Identify the blood parasite species.
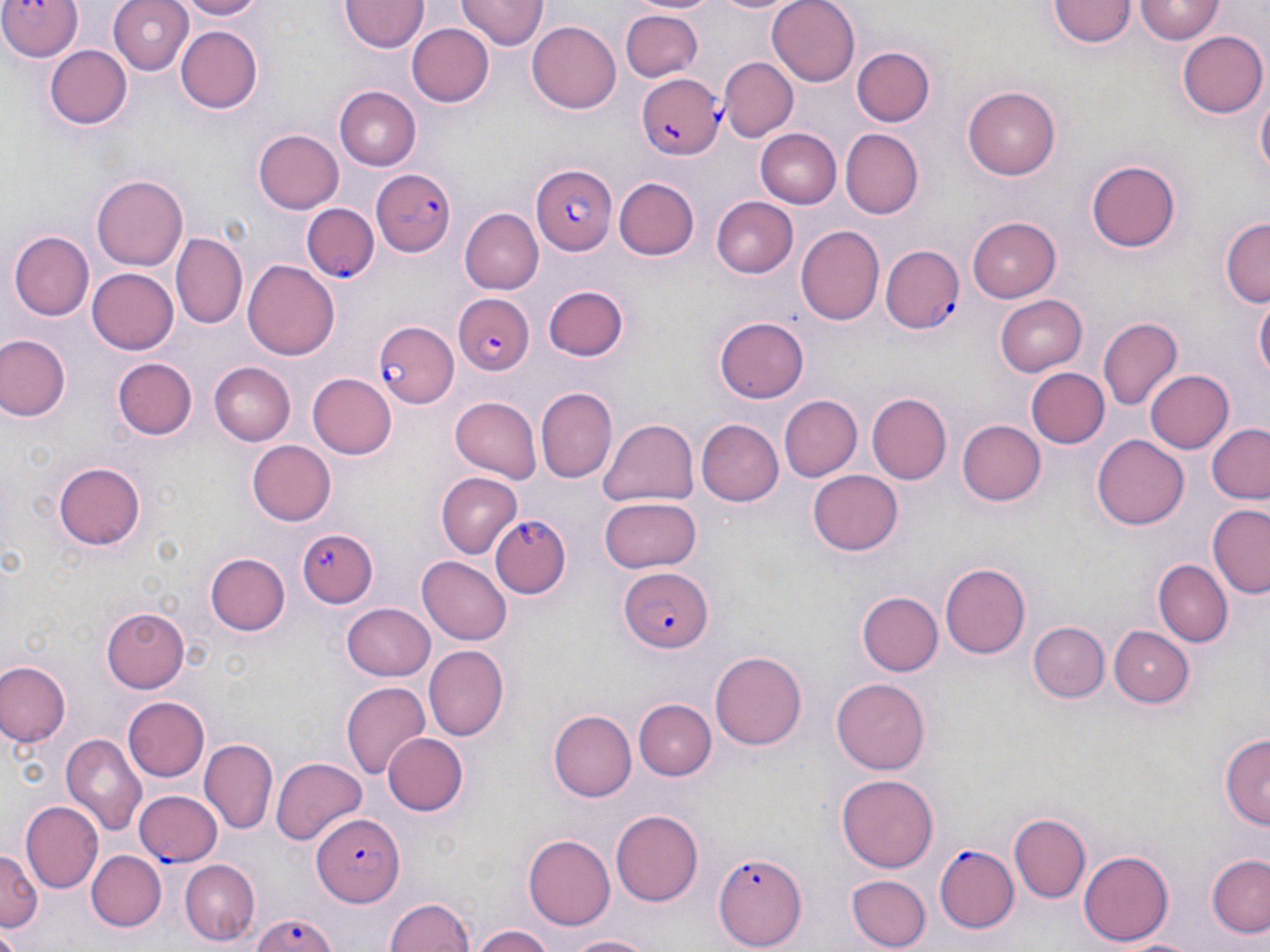

Plasmodium falciparum.

Approximate bounding boxes as named x1/y1/x2/y2 corners in pixels. Uninfected red blood cell locations: (x1=107, y1=0, x2=195, y2=74), (x1=175, y1=0, x2=265, y2=20), (x1=458, y1=0, x2=546, y2=52), (x1=635, y1=0, x2=718, y2=16), (x1=709, y1=0, x2=797, y2=16), (x1=767, y1=0, x2=861, y2=86), (x1=1051, y1=0, x2=1133, y2=49), (x1=1136, y1=1, x2=1224, y2=44), (x1=340, y1=2, x2=426, y2=54), (x1=620, y1=7, x2=702, y2=80), (x1=527, y1=21, x2=622, y2=113), (x1=408, y1=23, x2=494, y2=107), (x1=175, y1=24, x2=263, y2=114), (x1=1179, y1=30, x2=1268, y2=118), (x1=45, y1=43, x2=132, y2=130), (x1=851, y1=46, x2=936, y2=126), (x1=718, y1=57, x2=797, y2=142), (x1=964, y1=86, x2=1062, y2=179), (x1=334, y1=87, x2=420, y2=171), (x1=1255, y1=93, x2=1269, y2=184), (x1=840, y1=127, x2=923, y2=217), (x1=252, y1=129, x2=343, y2=214), (x1=755, y1=129, x2=842, y2=207), (x1=1087, y1=157, x2=1182, y2=251), (x1=93, y1=175, x2=188, y2=271), (x1=613, y1=177, x2=699, y2=261), (x1=710, y1=195, x2=797, y2=276), (x1=459, y1=206, x2=543, y2=291), (x1=966, y1=215, x2=1060, y2=304), (x1=1221, y1=219, x2=1269, y2=308), (x1=796, y1=226, x2=885, y2=327), (x1=172, y1=230, x2=246, y2=329), (x1=11, y1=231, x2=94, y2=320), (x1=244, y1=260, x2=339, y2=361), (x1=87, y1=267, x2=178, y2=355), (x1=543, y1=287, x2=627, y2=362), (x1=994, y1=292, x2=1088, y2=374), (x1=1255, y1=295, x2=1269, y2=386), (x1=713, y1=316, x2=809, y2=404), (x1=1099, y1=318, x2=1182, y2=410), (x1=0, y1=333, x2=70, y2=421), (x1=111, y1=356, x2=198, y2=443), (x1=206, y1=362, x2=295, y2=447), (x1=1027, y1=367, x2=1109, y2=449), (x1=1145, y1=369, x2=1235, y2=454), (x1=308, y1=373, x2=397, y2=459), (x1=537, y1=385, x2=616, y2=482), (x1=867, y1=392, x2=952, y2=483), (x1=779, y1=394, x2=861, y2=482), (x1=449, y1=397, x2=543, y2=482), (x1=598, y1=416, x2=699, y2=509), (x1=695, y1=420, x2=781, y2=505), (x1=955, y1=421, x2=1046, y2=508), (x1=1207, y1=424, x2=1270, y2=506), (x1=1092, y1=433, x2=1190, y2=530), (x1=246, y1=440, x2=337, y2=526), (x1=54, y1=462, x2=144, y2=550), (x1=808, y1=468, x2=904, y2=555), (x1=437, y1=473, x2=522, y2=558), (x1=599, y1=496, x2=703, y2=575), (x1=1207, y1=505, x2=1270, y2=597), (x1=205, y1=550, x2=290, y2=636), (x1=417, y1=556, x2=512, y2=644), (x1=1154, y1=560, x2=1231, y2=646), (x1=942, y1=562, x2=1033, y2=659), (x1=856, y1=591, x2=941, y2=677), (x1=341, y1=603, x2=436, y2=680), (x1=102, y1=608, x2=189, y2=692), (x1=1028, y1=622, x2=1110, y2=703), (x1=1110, y1=626, x2=1193, y2=705), (x1=424, y1=646, x2=509, y2=741), (x1=710, y1=650, x2=807, y2=750), (x1=0, y1=661, x2=70, y2=748), (x1=832, y1=679, x2=929, y2=775), (x1=341, y1=680, x2=431, y2=781), (x1=121, y1=695, x2=210, y2=783), (x1=632, y1=698, x2=716, y2=780), (x1=549, y1=710, x2=636, y2=804), (x1=1218, y1=731, x2=1270, y2=828), (x1=381, y1=732, x2=467, y2=817), (x1=60, y1=735, x2=146, y2=835), (x1=202, y1=740, x2=278, y2=834), (x1=270, y1=755, x2=366, y2=845), (x1=835, y1=773, x2=939, y2=875), (x1=22, y1=802, x2=103, y2=894), (x1=611, y1=809, x2=705, y2=904), (x1=1010, y1=813, x2=1091, y2=902), (x1=523, y1=834, x2=617, y2=931), (x1=1080, y1=848, x2=1174, y2=945), (x1=0, y1=851, x2=41, y2=932), (x1=86, y1=851, x2=166, y2=934), (x1=1207, y1=853, x2=1270, y2=940), (x1=180, y1=859, x2=260, y2=943), (x1=848, y1=873, x2=931, y2=949), (x1=383, y1=896, x2=476, y2=952), (x1=472, y1=925, x2=557, y2=952), (x1=0, y1=928, x2=22, y2=951), (x1=557, y1=932, x2=662, y2=951). Plasmodium falciparum-infected red blood cell locations: (x1=0, y1=0, x2=81, y2=60), (x1=635, y1=72, x2=721, y2=158), (x1=532, y1=163, x2=616, y2=257), (x1=370, y1=168, x2=458, y2=259), (x1=301, y1=204, x2=378, y2=283), (x1=883, y1=246, x2=964, y2=334), (x1=458, y1=294, x2=535, y2=376), (x1=372, y1=321, x2=457, y2=406), (x1=490, y1=516, x2=572, y2=601), (x1=298, y1=528, x2=380, y2=608), (x1=620, y1=568, x2=712, y2=652), (x1=135, y1=788, x2=224, y2=867), (x1=311, y1=808, x2=402, y2=905), (x1=933, y1=843, x2=1019, y2=932), (x1=713, y1=851, x2=804, y2=950), (x1=243, y1=910, x2=344, y2=952). Captured at 1000x magnification. Single field of view. May-Grünwald-Giemsa-stained preparation. Thin blood film. Optical microscopy. Image is 1270×952 pixels.